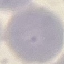
Result: no malaria parasites detected. Photographed with a smartphone camera at the microscope eyepiece. Giemsa-stained preparation. Thin smear of blood. Cell patch, automatically extracted from a larger field of view and resized to 64 × 64 pixels.